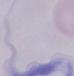

identification = trypanosome
modality = photomicrograph
magnification = 1000x